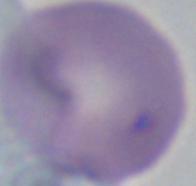

1000x magnification. A Babesia parasite is seen. Photomicrograph.